Point out each Plasmodium parasite.
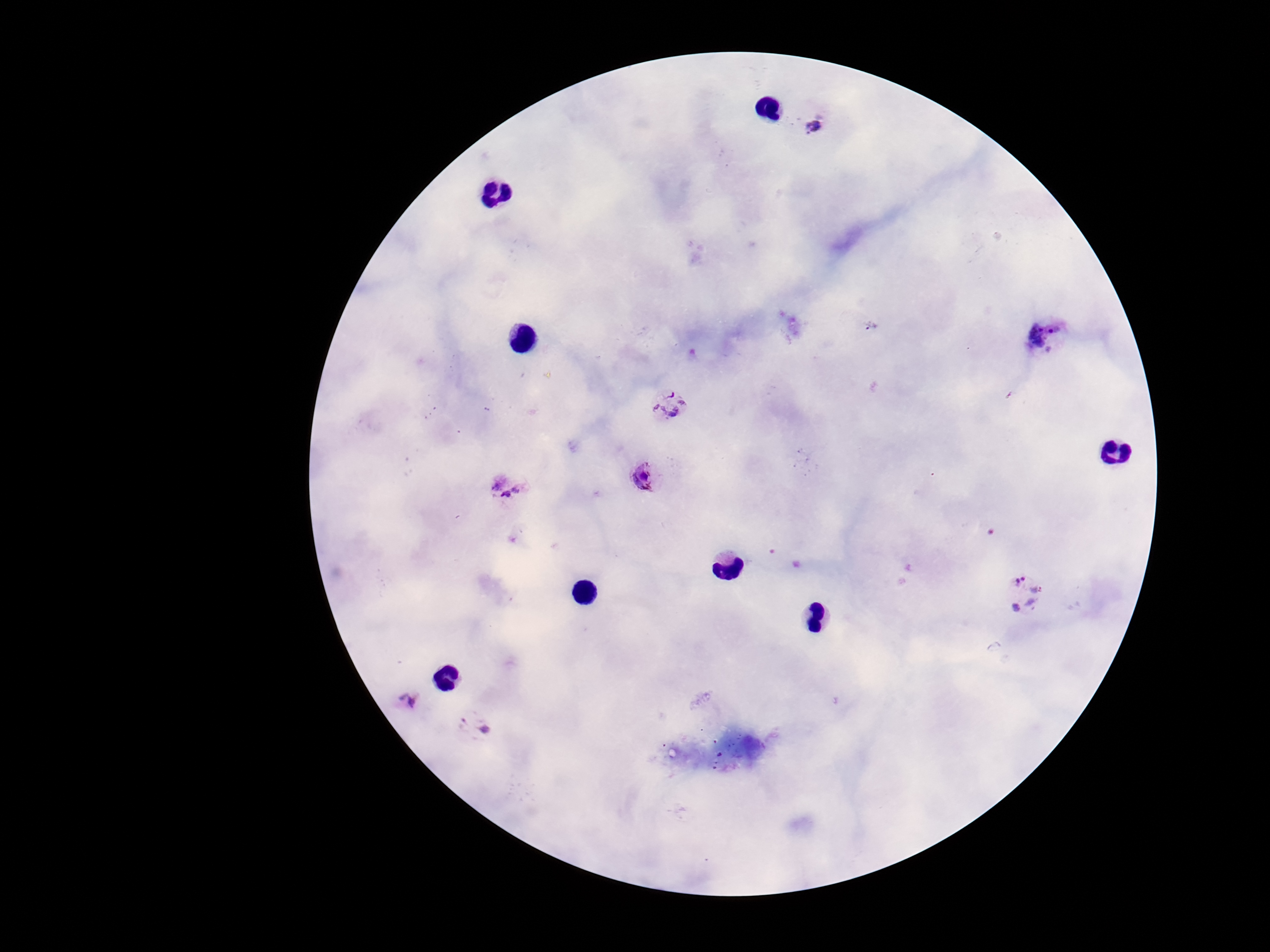
Approximate centers as {x, y} in pixels.
Plasmodium parasites: {820, 125}, {1049, 336}, {668, 405}, {646, 479}, {508, 487}, {1024, 593}, {408, 700}, {473, 725}.

stain: Giemsa
preparation: thick blood smear
field_of_view: one from this slide
image_size: 1270×952 pixels
magnification: 100x
capture: smartphone camera through the microscope eyepiece
patient_malaria_status: positive